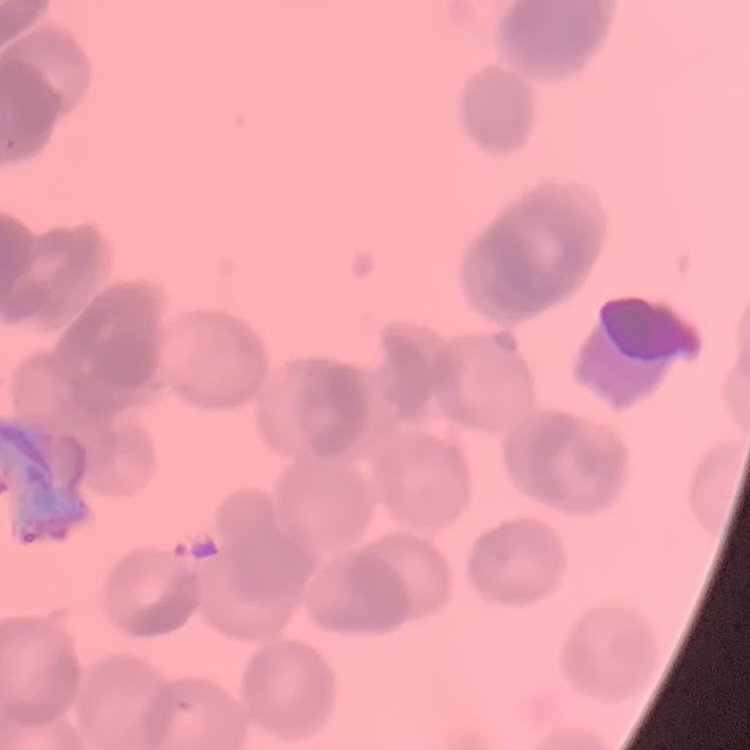

Summary:
  - Red blood cell morphology: rouleaux formation
  - Preparation: thin blood film
  - Stain: Field's or Giemsa
  - Image type: one tile cut from a larger photomicrograph